State the blood parasite species.
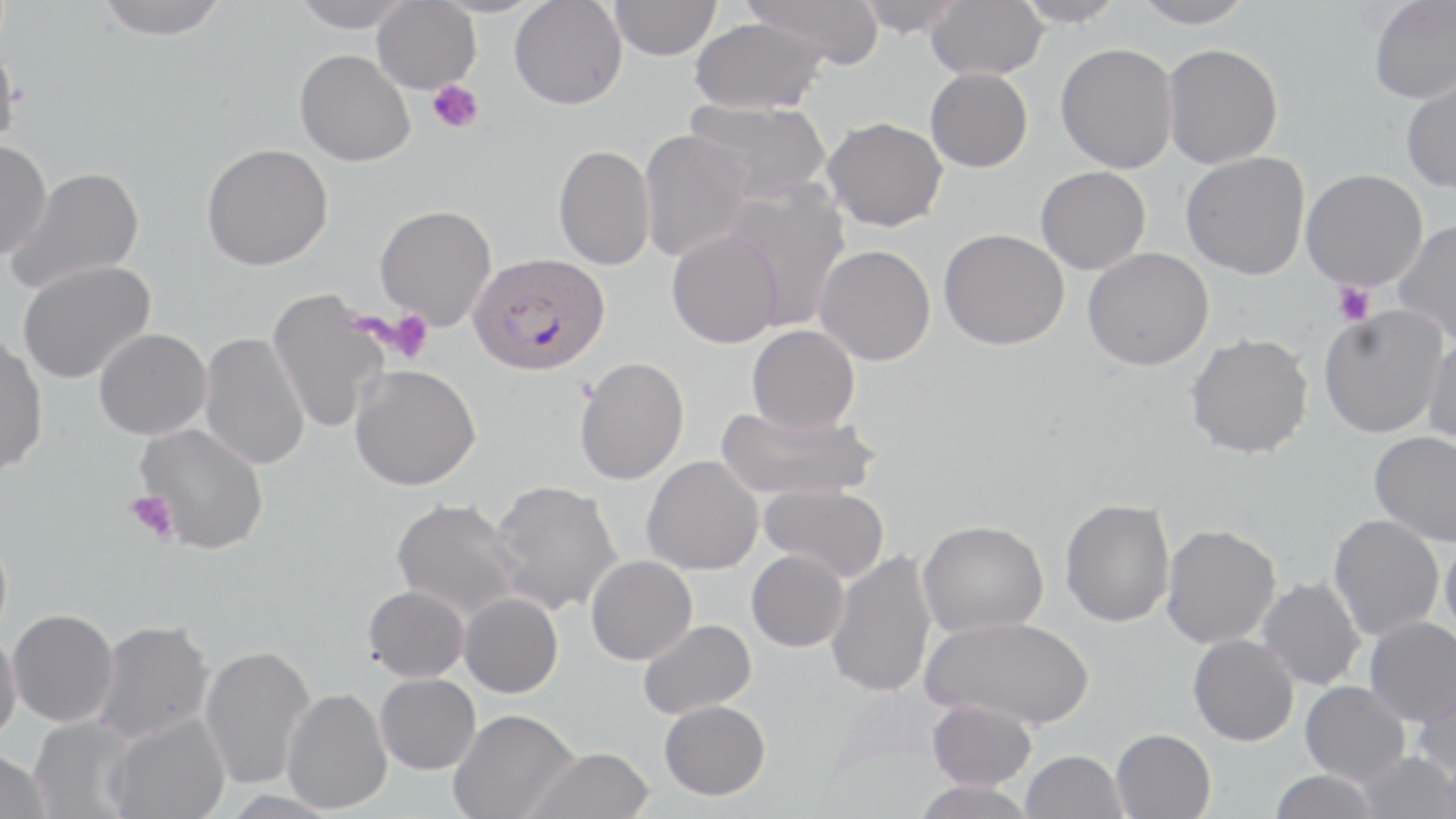

Plasmodium falciparum.

uninfected_red_blood_cell_locations: 'approximate bounding boxes as named x1/y1/x2/y2 corners in pixels: (x1=96, y1=0, x2=228, y2=40), (x1=291, y1=0, x2=415, y2=32), (x1=372, y1=0, x2=480, y2=93), (x1=509, y1=0, x2=627, y2=110), (x1=742, y1=0, x2=885, y2=68), (x1=855, y1=0, x2=965, y2=37), (x1=926, y1=0, x2=1048, y2=79), (x1=1014, y1=0, x2=1128, y2=27), (x1=1130, y1=0, x2=1256, y2=28), (x1=1367, y1=0, x2=1456, y2=104), (x1=609, y1=1, x2=721, y2=60), (x1=689, y1=16, x2=826, y2=114), (x1=0, y1=40, x2=24, y2=152), (x1=1054, y1=43, x2=1178, y2=173), (x1=1161, y1=43, x2=1283, y2=169), (x1=294, y1=50, x2=414, y2=166), (x1=925, y1=68, x2=1032, y2=172), (x1=1400, y1=74, x2=1456, y2=194), (x1=682, y1=98, x2=830, y2=204), (x1=822, y1=117, x2=947, y2=231), (x1=637, y1=129, x2=752, y2=262), (x1=0, y1=140, x2=51, y2=260), (x1=201, y1=143, x2=332, y2=270), (x1=553, y1=144, x2=656, y2=270), (x1=1179, y1=151, x2=1310, y2=280), (x1=1035, y1=166, x2=1151, y2=274), (x1=6, y1=167, x2=144, y2=294), (x1=1300, y1=169, x2=1427, y2=291), (x1=718, y1=181, x2=851, y2=332), (x1=374, y1=204, x2=497, y2=330), (x1=1392, y1=220, x2=1456, y2=347), (x1=938, y1=228, x2=1069, y2=350), (x1=666, y1=231, x2=783, y2=348), (x1=813, y1=244, x2=935, y2=366), (x1=1082, y1=247, x2=1213, y2=370), (x1=17, y1=260, x2=155, y2=384), (x1=266, y1=291, x2=390, y2=434), (x1=1318, y1=304, x2=1450, y2=439), (x1=745, y1=325, x2=860, y2=435), (x1=93, y1=328, x2=211, y2=441), (x1=199, y1=331, x2=310, y2=472), (x1=1185, y1=333, x2=1314, y2=459), (x1=1423, y1=335, x2=1456, y2=450), (x1=0, y1=336, x2=47, y2=476), (x1=573, y1=357, x2=689, y2=485), (x1=349, y1=364, x2=480, y2=491), (x1=716, y1=403, x2=877, y2=503), (x1=134, y1=423, x2=269, y2=553), (x1=1369, y1=431, x2=1456, y2=547), (x1=641, y1=455, x2=764, y2=575), (x1=490, y1=479, x2=622, y2=614), (x1=758, y1=484, x2=890, y2=583), (x1=391, y1=498, x2=523, y2=621), (x1=1060, y1=498, x2=1175, y2=627), (x1=1328, y1=514, x2=1444, y2=640), (x1=917, y1=520, x2=1048, y2=637), (x1=1161, y1=524, x2=1280, y2=649), (x1=1440, y1=531, x2=1456, y2=644), (x1=825, y1=549, x2=936, y2=698), (x1=746, y1=550, x2=849, y2=652), (x1=586, y1=555, x2=697, y2=665), (x1=1257, y1=577, x2=1366, y2=691), (x1=363, y1=585, x2=469, y2=681), (x1=459, y1=593, x2=563, y2=698), (x1=7, y1=609, x2=118, y2=727), (x1=921, y1=615, x2=1095, y2=729), (x1=1364, y1=616, x2=1456, y2=725), (x1=93, y1=619, x2=214, y2=744), (x1=637, y1=619, x2=756, y2=718), (x1=0, y1=630, x2=21, y2=744), (x1=1188, y1=634, x2=1298, y2=745), (x1=199, y1=644, x2=316, y2=790), (x1=1414, y1=670, x2=1456, y2=783), (x1=374, y1=673, x2=480, y2=774), (x1=1300, y1=680, x2=1410, y2=785), (x1=281, y1=687, x2=392, y2=814), (x1=926, y1=699, x2=1036, y2=790), (x1=659, y1=700, x2=771, y2=800), (x1=448, y1=708, x2=579, y2=819), (x1=106, y1=713, x2=230, y2=819), (x1=29, y1=716, x2=140, y2=819), (x1=1111, y1=728, x2=1215, y2=819), (x1=523, y1=747, x2=654, y2=819), (x1=0, y1=749, x2=51, y2=819), (x1=1020, y1=750, x2=1127, y2=819), (x1=1355, y1=751, x2=1456, y2=819), (x1=1269, y1=770, x2=1378, y2=819), (x1=911, y1=780, x2=1037, y2=819)'
plasmodium_falciparum_infected_red_blood_cell_locations: 'approximate bounding boxes as named x1/y1/x2/y2 corners in pixels: (x1=468, y1=252, x2=609, y2=375)'
image_size: 1456×819 pixels
magnification: 1000x
stain: May-Grünwald-Giemsa
platelet_locations: 'approximate bounding boxes as named x1/y1/x2/y2 corners in pixels: (x1=427, y1=80, x2=484, y2=134), (x1=1331, y1=282, x2=1375, y2=326), (x1=385, y1=309, x2=433, y2=365), (x1=124, y1=490, x2=179, y2=544)'
preparation: thin blood film
modality: light microscopy
field_of_view: single